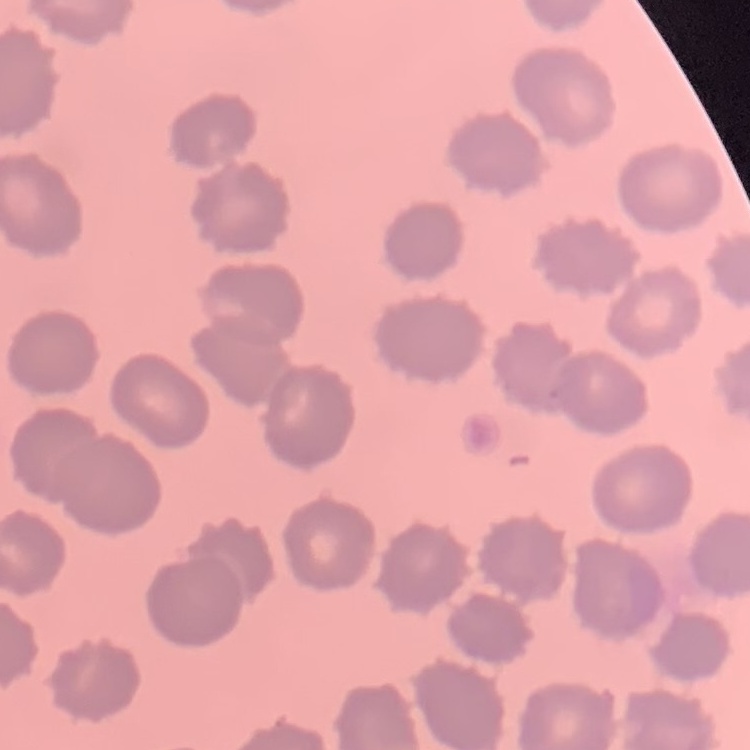

Summary:
  - Red blood cell morphology: no rouleaux formation
  - Stain: Field's or Giemsa
  - Preparation: thin blood smear
  - Image type: one tile cut from a larger photomicrograph